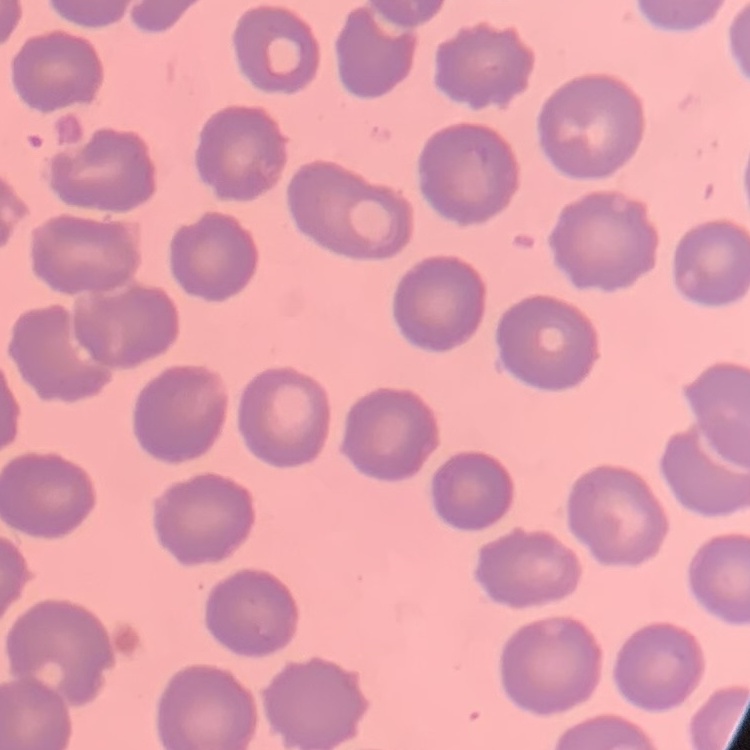

Summary:
  - Erythrocyte morphology: no rouleaux formation
  - Image type: square crop of a larger photomicrograph
  - Preparation: thin peripheral smear
  - Stain: Field's or Giemsa